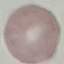
result = negative for malaria parasites
stain = Giemsa
capture = smartphone through the microscope eyepiece
image type = automatically extracted cell patch, resized to 64 × 64 pixels
preparation = thin blood film